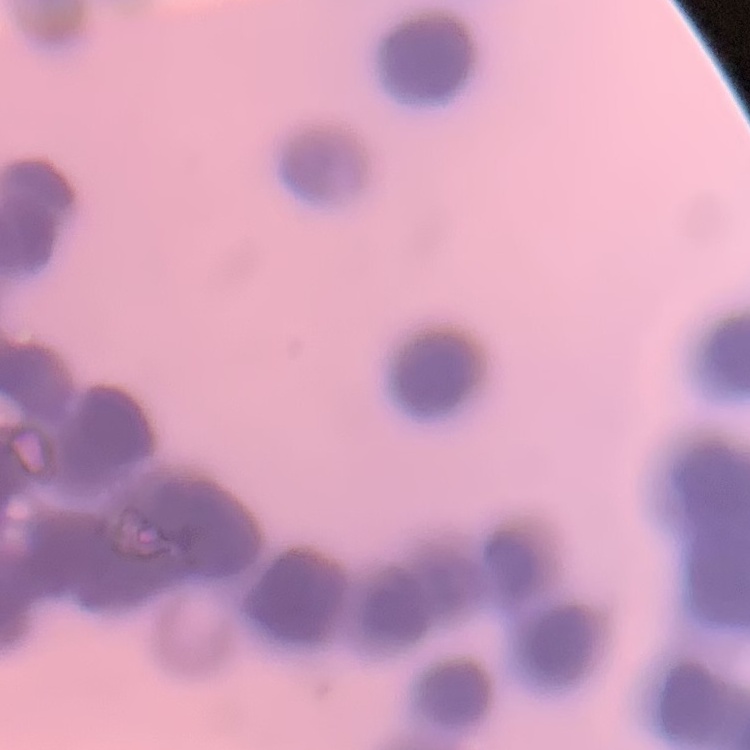
The erythrocytes exhibit rouleaux formation. Thin peripheral smear. Square crop of a larger photomicrograph. Stained with either Field's or Giemsa.